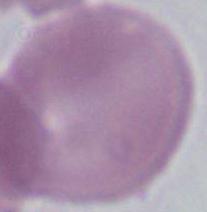
{
  "identification": "red blood cell",
  "modality": "micrograph",
  "magnification": "1000x"
}